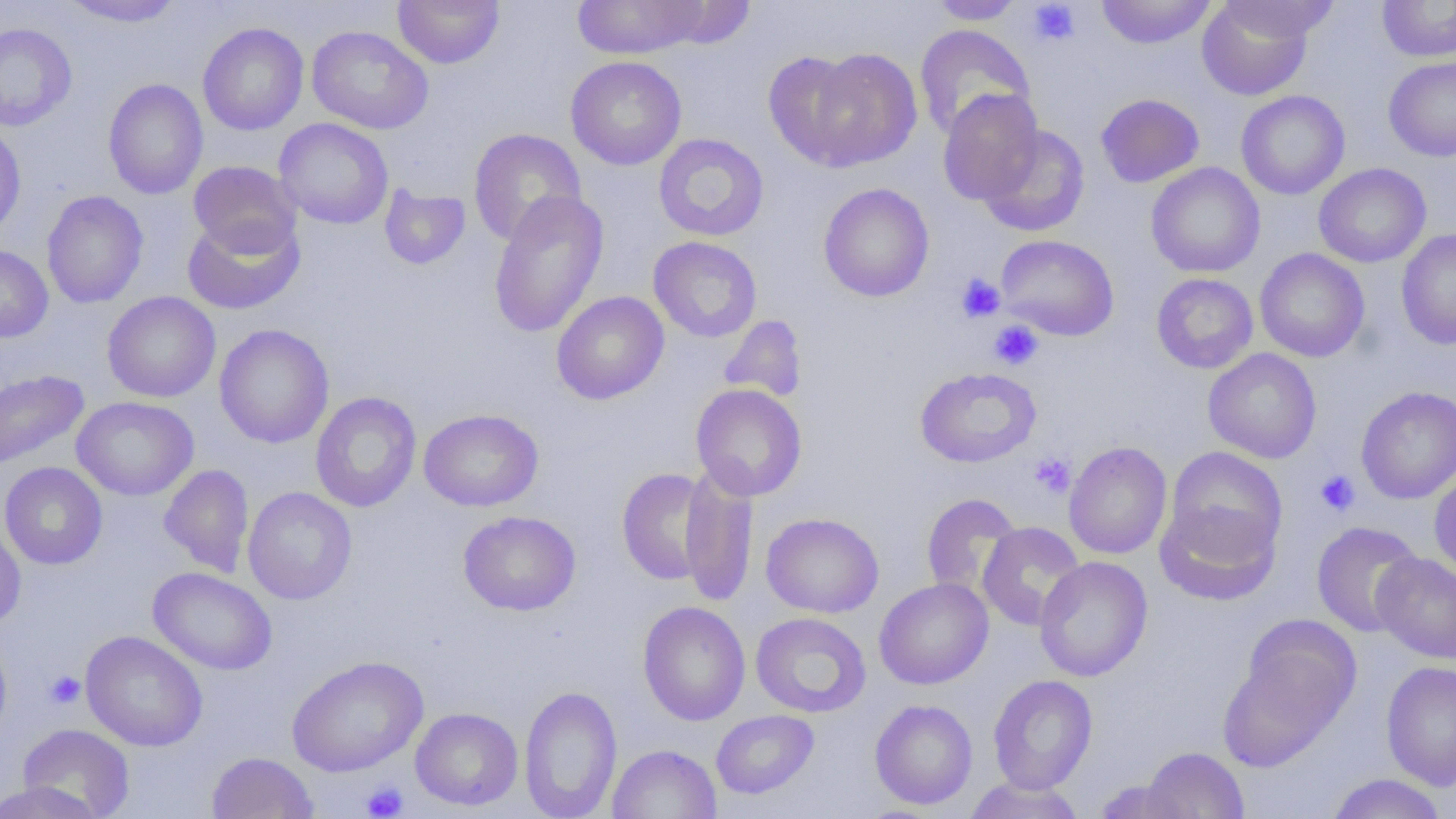

{
  "slide_level_diagnosis": "no evidence of blood parasites",
  "field_of_view": "one of a larger specimen",
  "uninfected_red_blood_cell_locations": "approximate bounding boxes as (x1,y1)-(x2,y2) corner pairs in pixels: (60,0)-(186,28), (392,0)-(505,68), (572,0)-(706,59), (1096,0)-(1217,49), (1222,0)-(1341,42), (1377,0)-(1456,61), (649,1)-(757,49), (928,1)-(1027,25), (1197,1)-(1313,100), (197,22)-(309,136), (0,23)-(77,132), (914,24)-(1036,139), (306,25)-(433,134), (762,49)-(867,169), (802,49)-(922,171), (565,56)-(687,171), (1383,56)-(1456,162), (102,78)-(209,199), (937,89)-(1045,206), (1236,90)-(1350,200), (1095,93)-(1205,188), (273,118)-(394,229), (0,121)-(26,240), (978,124)-(1090,237), (468,128)-(586,247), (653,133)-(769,241), (188,160)-(301,257), (1146,162)-(1265,277), (1314,163)-(1431,267), (818,182)-(934,302), (379,185)-(471,270), (488,189)-(609,339), (41,190)-(148,309), (182,214)-(305,315), (1396,228)-(1456,350), (996,234)-(1119,341), (648,236)-(762,342), (0,244)-(53,342), (1254,248)-(1370,362), (1151,273)-(1258,374), (102,291)-(221,402), (551,291)-(669,405), (718,314)-(807,403), (213,323)-(334,449), (1203,348)-(1322,464), (915,367)-(1042,468), (0,368)-(90,471), (691,383)-(807,501), (1356,386)-(1456,504), (310,392)-(421,513), (71,396)-(199,501), (419,409)-(543,511), (1063,441)-(1172,559), (1165,448)-(1287,564), (0,462)-(108,570), (159,464)-(254,577), (616,468)-(720,587), (1429,468)-(1456,579), (679,471)-(758,606), (243,487)-(357,605), (921,493)-(1022,599), (1155,499)-(1280,606), (458,510)-(581,616), (761,512)-(884,618), (0,519)-(26,630), (977,521)-(1086,631), (1311,521)-(1425,637), (1371,552)-(1456,664), (1034,555)-(1153,682), (148,567)-(278,675), (874,577)-(993,689), (638,601)-(751,726), (751,612)-(871,718), (1242,615)-(1361,730), (80,630)-(208,752), (0,634)-(12,746), (287,655)-(428,777), (1216,655)-(1343,771), (1381,660)-(1456,791), (987,674)-(1097,794), (519,685)-(622,819), (870,699)-(978,809), (410,707)-(523,811), (710,710)-(819,800), (17,723)-(135,816), (607,744)-(721,819), (1142,746)-(1248,818), (207,751)-(318,818), (1326,773)-(1447,819), (963,776)-(1085,819), (1092,778)-(1192,818), (0,780)-(107,819)",
  "platelet_locations": "approximate bounding boxes as (x1,y1)-(x2,y2) corner pairs in pixels: (1028,1)-(1080,46), (956,273)-(1005,323), (989,320)-(1043,370), (1030,451)-(1076,498), (1315,469)-(1360,516), (45,671)-(85,709), (361,780)-(409,819)",
  "magnification": "1000x",
  "image_size": "1456×819 pixels",
  "preparation": "thin blood smear",
  "modality": "optical microscopy"
}